Classify this cell by malaria status.
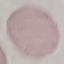

Uninfected.

Summary:
  - Capture: smartphone camera at the microscope eyepiece
  - Image type: automatically extracted cell patch, resized to 64 × 64 pixels
  - Stain: Giemsa
  - Preparation: thin smear